Identify the preparation type.
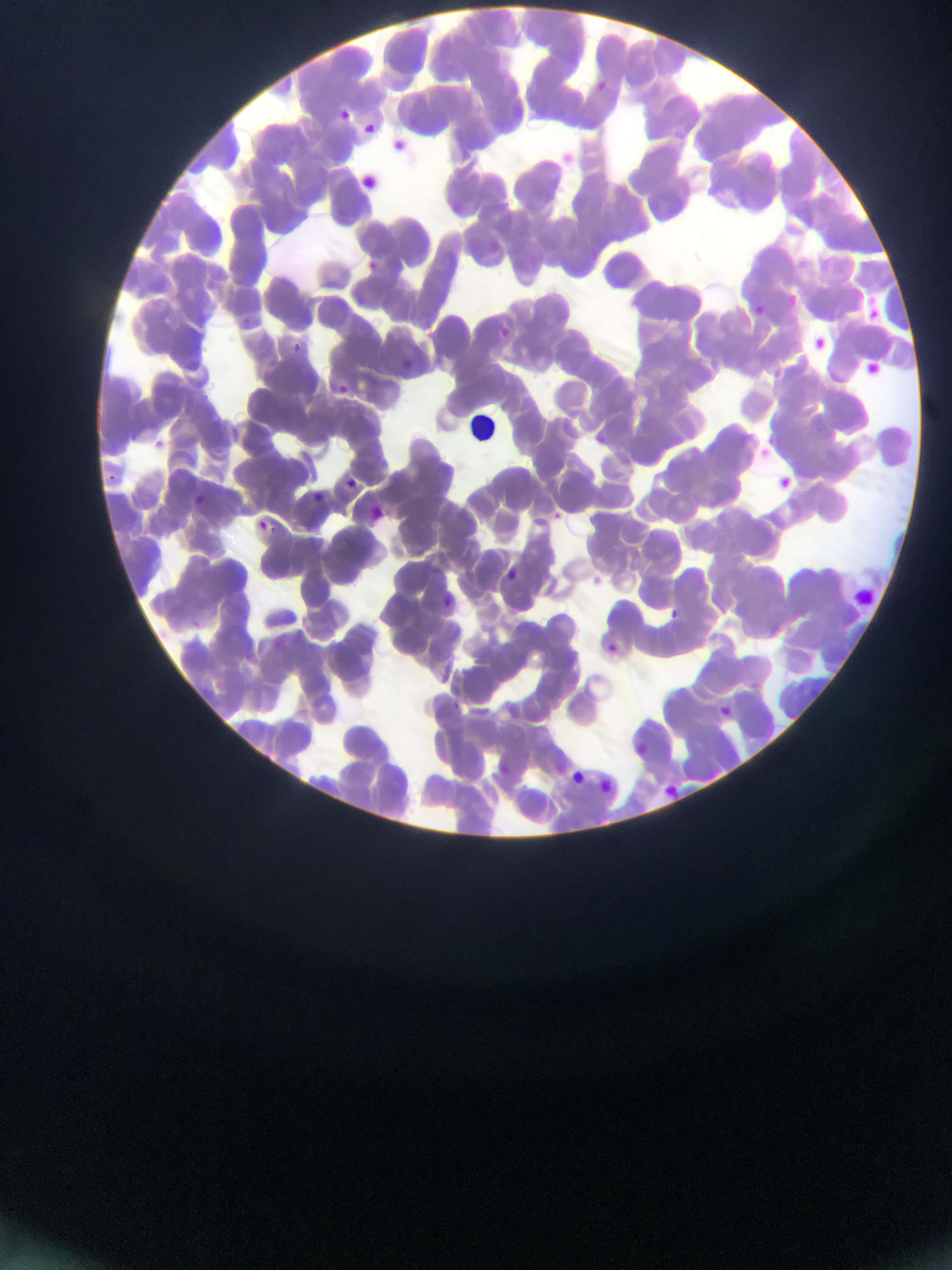
Thin blood smear.

capture: mobile-phone photograph through a microscope
leukocyte_locations: 'approximate bounding boxes as (left, top, right, bottom) in pixels: (847, 587, 869, 610)'
country: Ghana
field_of_view: single
image_size: 952×1270 pixels
plasmodium_parasite_locations: 'approximate bounding boxes as (left, top, right, bottom) in pixels: (589, 78, 612, 98), (333, 106, 353, 127), (358, 117, 380, 139), (391, 138, 410, 155), (363, 261, 376, 273), (784, 291, 801, 309), (746, 301, 768, 320), (496, 325, 513, 340), (290, 342, 303, 354), (397, 360, 421, 381), (330, 379, 352, 399), (590, 431, 601, 445), (142, 436, 168, 454), (753, 442, 773, 461), (103, 470, 122, 489), (345, 474, 375, 496), (774, 475, 798, 496), (306, 489, 328, 507), (165, 492, 203, 524), (551, 507, 565, 522), (370, 509, 383, 519), (253, 517, 271, 536), (501, 565, 522, 585), (593, 576, 603, 598), (439, 587, 456, 612), (666, 606, 682, 621), (609, 642, 628, 658), (715, 701, 735, 720), (623, 741, 657, 762), (566, 769, 589, 789), (598, 778, 617, 797), (662, 782, 687, 804), (589, 865, 597, 868)'